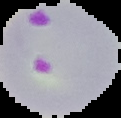
The area outside the segmented cell region is set to black. Image is 121×118 pixels. From a thin blood film. Malaria status: parasitized.